Describe the morphology of the erythrocytes.
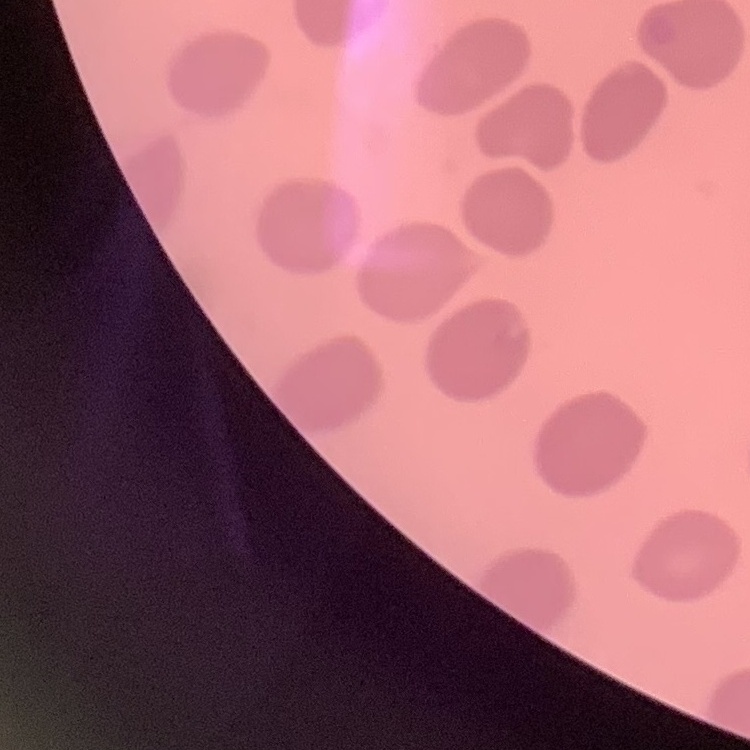

No rouleaux formation.

Summary:
  - Preparation: thin blood film
  - Image type: one tile cut from a larger photomicrograph
  - Stain: Field's or Giemsa